Assess for malaria.
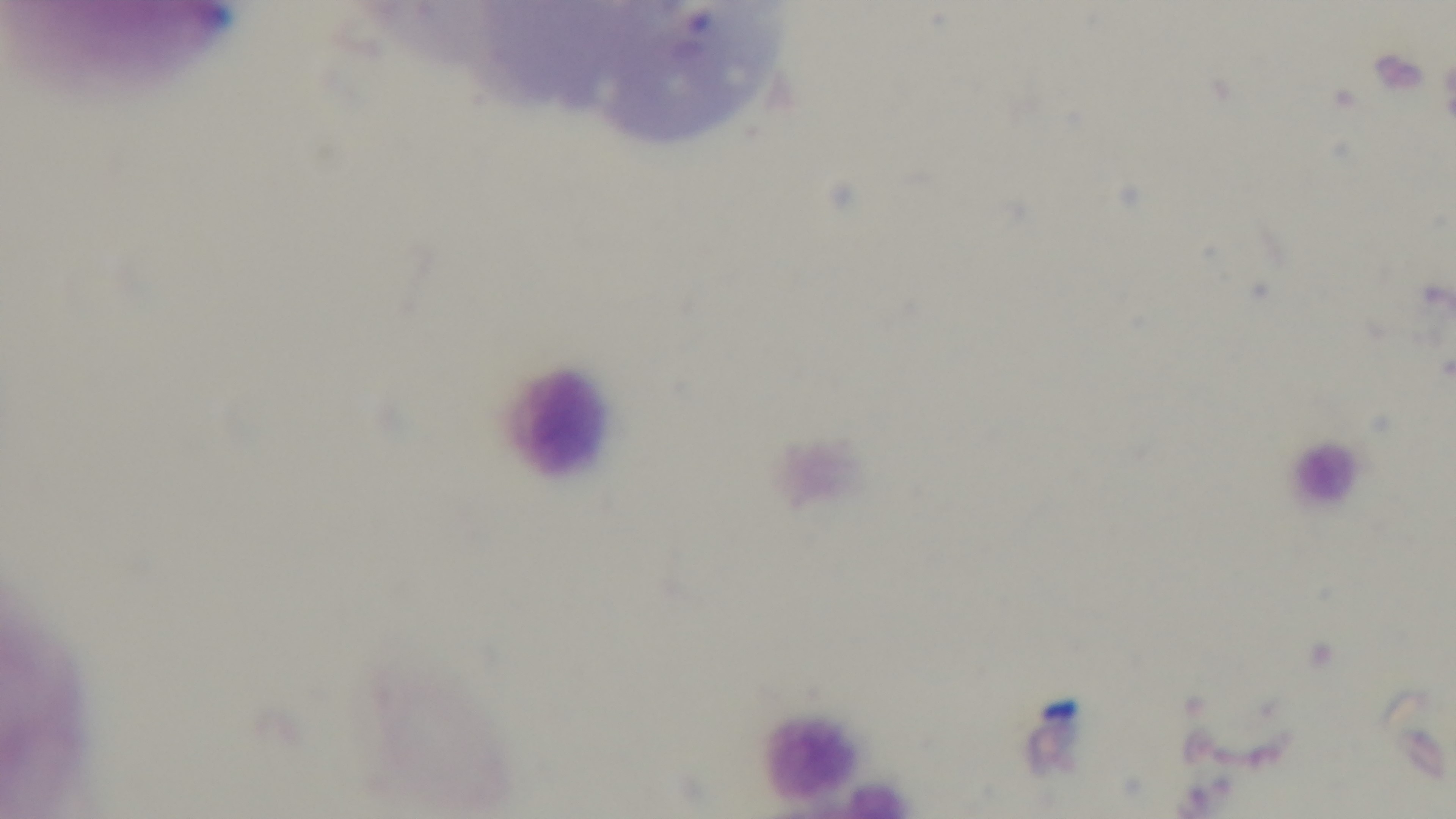
Negative.

objective = 100x oil immersion
preparation = thick smear
stain = Giemsa
field of view = one from the slide
modality = light microscopy
capture = mounted 4K digital camera